Locate every uninfected red blood cell.
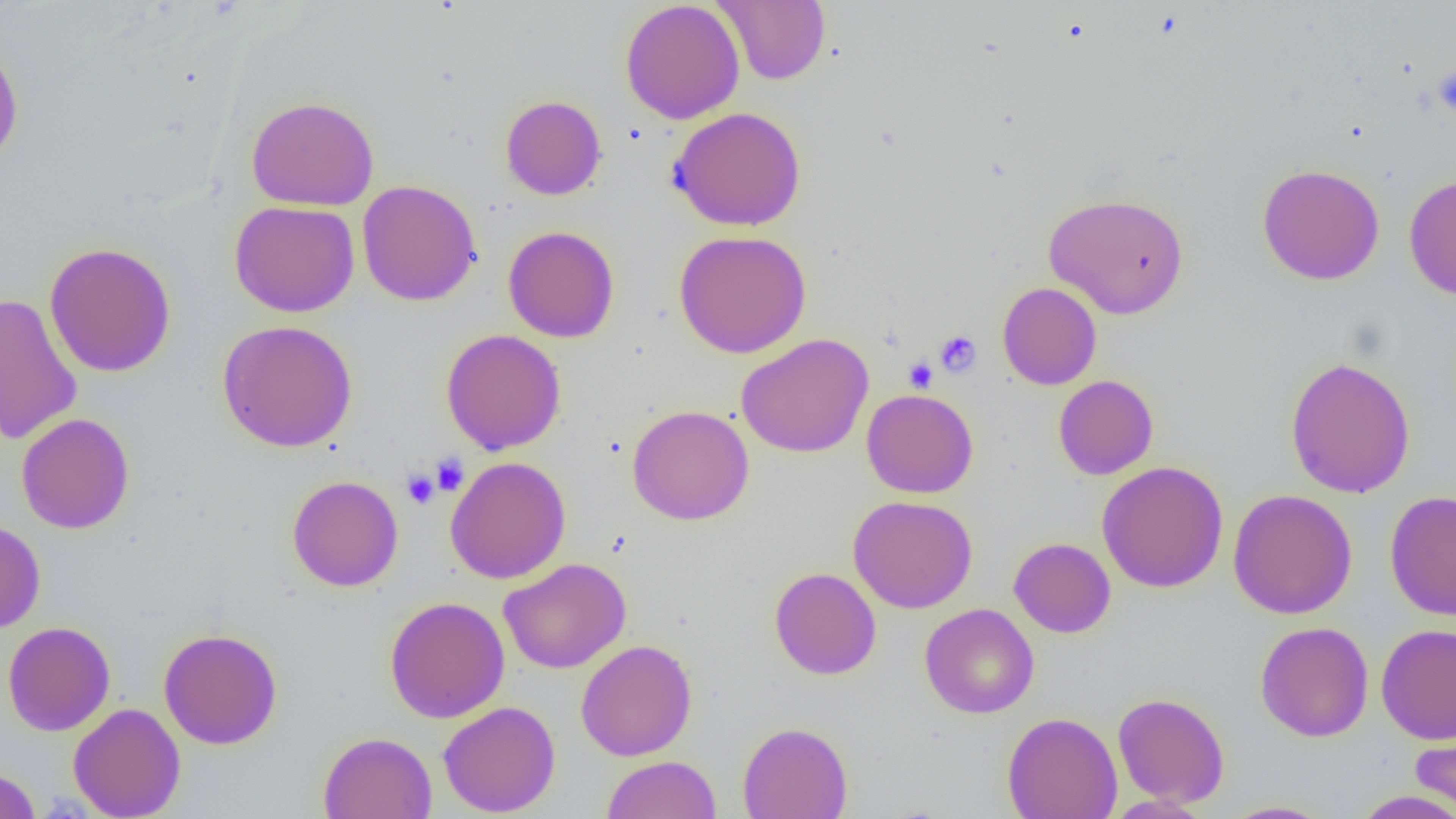

Approximate bounding boxes as [x1, y1, x2, y2] in pixels.
Uninfected red blood cells: [620, 0, 745, 124], [714, 0, 830, 85], [0, 39, 24, 169], [500, 95, 607, 200], [246, 96, 380, 211], [668, 106, 806, 231], [1257, 163, 1385, 285], [1403, 174, 1456, 301], [357, 180, 482, 306], [1043, 192, 1189, 318], [229, 200, 359, 318], [503, 225, 619, 343], [674, 229, 812, 358], [44, 241, 177, 378], [997, 282, 1102, 390], [0, 293, 82, 446], [217, 319, 358, 452], [440, 329, 566, 455], [736, 333, 874, 458], [1284, 356, 1416, 498], [1053, 375, 1158, 480], [862, 389, 978, 498], [627, 405, 754, 525], [16, 412, 135, 534], [445, 456, 571, 584], [1096, 460, 1229, 593], [287, 475, 403, 592], [1228, 488, 1358, 620], [1385, 490, 1456, 620], [848, 495, 978, 614], [0, 520, 46, 634], [1008, 537, 1116, 638], [499, 558, 631, 674], [769, 567, 881, 679], [384, 595, 510, 722], [919, 603, 1039, 719], [2, 621, 116, 736], [1255, 621, 1374, 743], [1376, 623, 1456, 744], [159, 628, 283, 750], [576, 640, 697, 761], [1112, 691, 1230, 807], [438, 701, 560, 817], [68, 702, 185, 819], [1002, 711, 1123, 819], [1410, 718, 1456, 817], [738, 721, 852, 819], [318, 731, 437, 818], [602, 755, 721, 818], [0, 765, 41, 819], [1351, 790, 1456, 818], [1103, 795, 1212, 818], [1219, 800, 1336, 818].

Platelet locations: [1433, 64, 1456, 119], [935, 330, 981, 377], [905, 358, 937, 392], [431, 453, 469, 495], [402, 469, 439, 509]. Slide-level diagnosis: no evidence of blood parasites. 1000x magnification. Thin blood film. Light microscopy. Image is 1456×819 pixels. One field of a larger specimen.